State the blood parasite species.
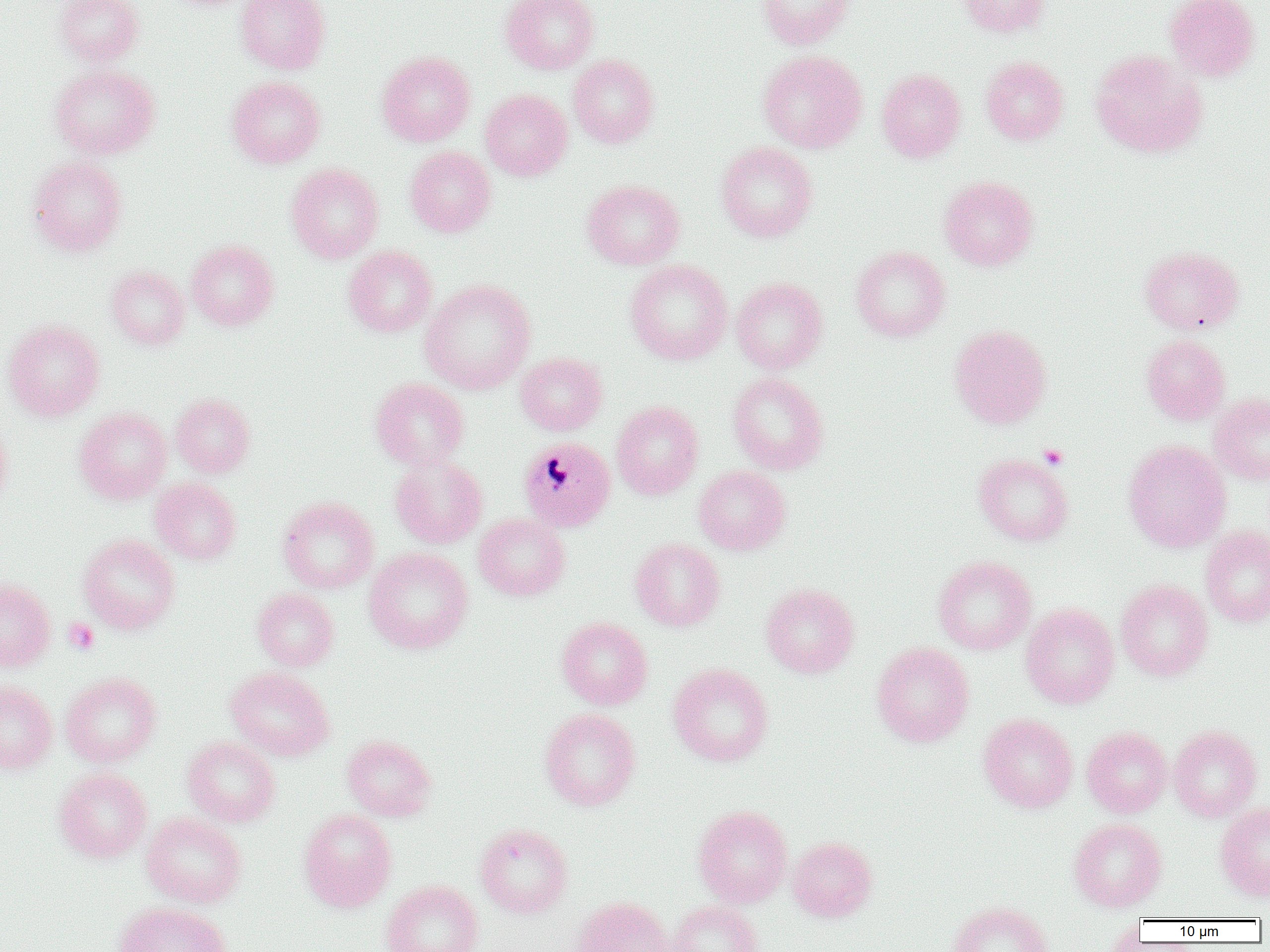

Plasmodium malariae.

Approximate bounding boxes as [x1, y1, x2, y2] in pixels. Uninfected red blood cell locations: [54, 0, 144, 66], [236, 0, 330, 74], [500, 0, 599, 74], [756, 0, 855, 50], [957, 0, 1051, 38], [1164, 0, 1261, 82], [1090, 49, 1207, 158], [376, 50, 475, 147], [757, 50, 867, 153], [567, 55, 659, 148], [981, 56, 1069, 146], [49, 64, 160, 158], [877, 68, 966, 162], [228, 76, 325, 168], [480, 88, 572, 181], [716, 142, 817, 242], [405, 146, 496, 238], [28, 155, 127, 257], [286, 163, 383, 263], [939, 175, 1039, 271], [582, 179, 685, 270], [186, 240, 279, 331], [343, 245, 437, 337], [850, 245, 951, 342], [1139, 245, 1244, 334], [625, 260, 732, 365], [106, 265, 189, 350], [730, 277, 828, 374], [420, 280, 536, 394], [3, 319, 105, 421], [948, 324, 1052, 429], [1141, 334, 1230, 425], [515, 352, 607, 435], [727, 372, 829, 475], [370, 377, 469, 470], [1209, 392, 1270, 485], [170, 393, 255, 478], [611, 401, 704, 500], [73, 407, 172, 504], [0, 420, 12, 508], [1123, 440, 1231, 553], [973, 453, 1073, 546], [390, 456, 487, 549], [693, 466, 791, 555], [150, 478, 241, 565], [278, 497, 378, 594], [473, 513, 570, 601], [1200, 526, 1270, 627], [78, 534, 180, 635], [629, 538, 725, 632], [364, 547, 474, 654], [933, 555, 1036, 654], [0, 576, 55, 672], [1116, 579, 1213, 681], [760, 582, 859, 678], [252, 587, 339, 671], [1021, 602, 1120, 709], [556, 617, 653, 710], [872, 642, 974, 747], [668, 663, 774, 766], [225, 667, 334, 761], [60, 672, 162, 768], [0, 681, 57, 774], [539, 708, 641, 811], [978, 713, 1078, 813], [1168, 725, 1262, 822], [1082, 726, 1172, 818], [343, 735, 436, 822], [182, 737, 281, 827], [54, 768, 151, 862], [1215, 802, 1270, 901], [692, 804, 793, 908], [298, 809, 397, 912], [141, 812, 247, 907], [1069, 818, 1167, 911], [475, 823, 573, 918], [788, 836, 877, 922], [381, 879, 484, 952], [572, 897, 674, 952], [666, 900, 762, 952], [947, 901, 1053, 952], [114, 902, 231, 952]. Plasmodium malariae-infected red blood cell locations: [519, 437, 616, 532]. Platelet locations: [1038, 444, 1069, 469], [63, 618, 99, 654]. Image is 1270×952 pixels. Thin blood smear. 1000x magnification. One field of a larger specimen. Optical microscopy.